Classify this cell by malaria status.
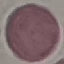
It is uninfected.

Summary:
  - Capture: smartphone camera at the microscope eyepiece
  - Stain: Giemsa
  - Image type: cell patch, automatically extracted from a larger field of view and resized to 64 × 64 pixels
  - Preparation: thin blood smear